State the blood parasite species.
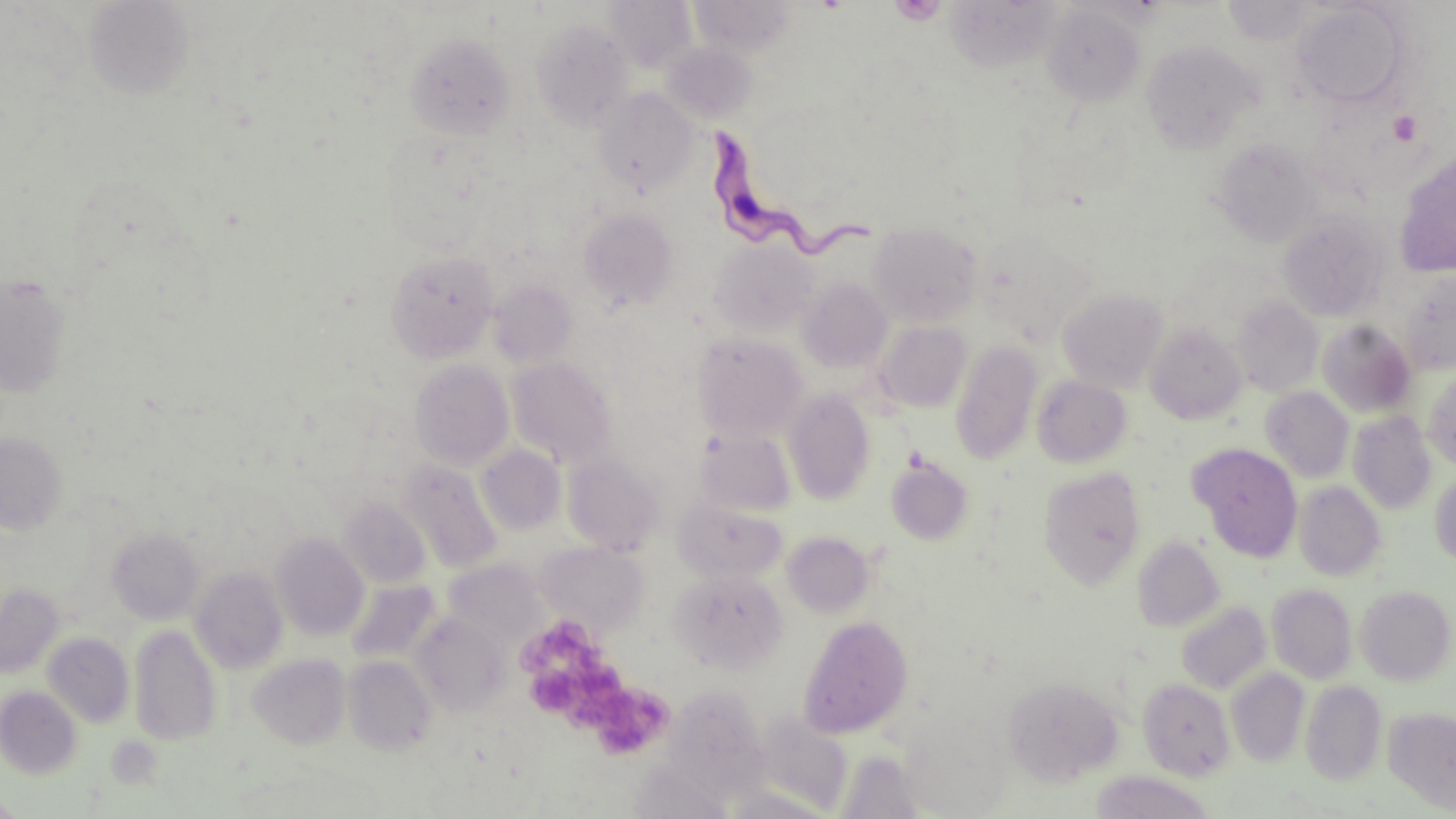

Trypanosoma brucei.

Approximate bounding boxes as (x1, y1, x2, y2) in pixels. Uninfected red blood cell locations: (687, 0, 797, 57), (604, 1, 697, 72), (1221, 1, 1323, 46), (84, 2, 195, 100), (1290, 2, 1411, 107), (1041, 4, 1145, 105), (530, 17, 635, 131), (406, 31, 516, 140), (1140, 40, 1260, 152), (660, 42, 758, 126), (594, 88, 699, 194), (1213, 139, 1321, 247), (1394, 153, 1456, 277), (577, 208, 678, 310), (1278, 210, 1391, 322), (867, 223, 982, 327), (979, 231, 1094, 340), (709, 237, 818, 337), (385, 250, 499, 363), (1399, 271, 1456, 375), (1, 276, 72, 396), (798, 278, 892, 373), (489, 281, 578, 368), (1058, 288, 1169, 392), (1232, 295, 1323, 397), (874, 321, 971, 413), (1318, 321, 1416, 417), (1145, 323, 1247, 424), (692, 332, 808, 440), (950, 341, 1043, 464), (506, 357, 617, 467), (410, 359, 514, 470), (1423, 368, 1456, 470), (1032, 375, 1132, 467), (1261, 387, 1354, 483), (783, 390, 876, 504), (1347, 411, 1437, 514), (696, 429, 796, 516), (0, 431, 67, 535), (1189, 443, 1303, 562), (477, 445, 566, 535), (562, 451, 666, 556), (885, 456, 973, 545), (399, 459, 502, 574), (1038, 466, 1147, 589), (1431, 468, 1456, 569), (1293, 480, 1386, 581), (340, 495, 432, 588), (674, 501, 787, 583), (107, 528, 204, 625), (782, 531, 876, 617), (271, 532, 369, 640), (1132, 536, 1225, 632), (535, 541, 648, 634), (442, 559, 548, 649), (189, 566, 288, 674), (669, 569, 788, 674), (345, 580, 442, 666), (0, 583, 64, 678), (1266, 583, 1358, 684), (1355, 585, 1455, 685), (1176, 600, 1271, 694), (410, 613, 509, 715), (798, 615, 914, 738), (129, 624, 223, 745), (43, 632, 134, 727), (248, 653, 351, 749), (343, 655, 437, 756), (1226, 668, 1310, 767), (1002, 676, 1125, 786), (1138, 678, 1235, 780), (1301, 680, 1387, 785), (673, 684, 770, 790), (0, 686, 83, 779), (1384, 706, 1456, 813), (753, 711, 854, 815), (833, 749, 932, 818), (626, 759, 735, 819), (1089, 771, 1217, 819), (719, 786, 837, 819), (1, 794, 24, 818). Trypanosoma brucei locations: (706, 129, 879, 263). Platelet locations: (888, 0, 949, 25), (1388, 110, 1424, 147), (527, 629, 668, 753), (524, 667, 578, 715). Light microscopy. Image is 1456×819 pixels. 1000x magnification. May-Grünwald-Giemsa-stained preparation. Thin blood film. Single field of view.